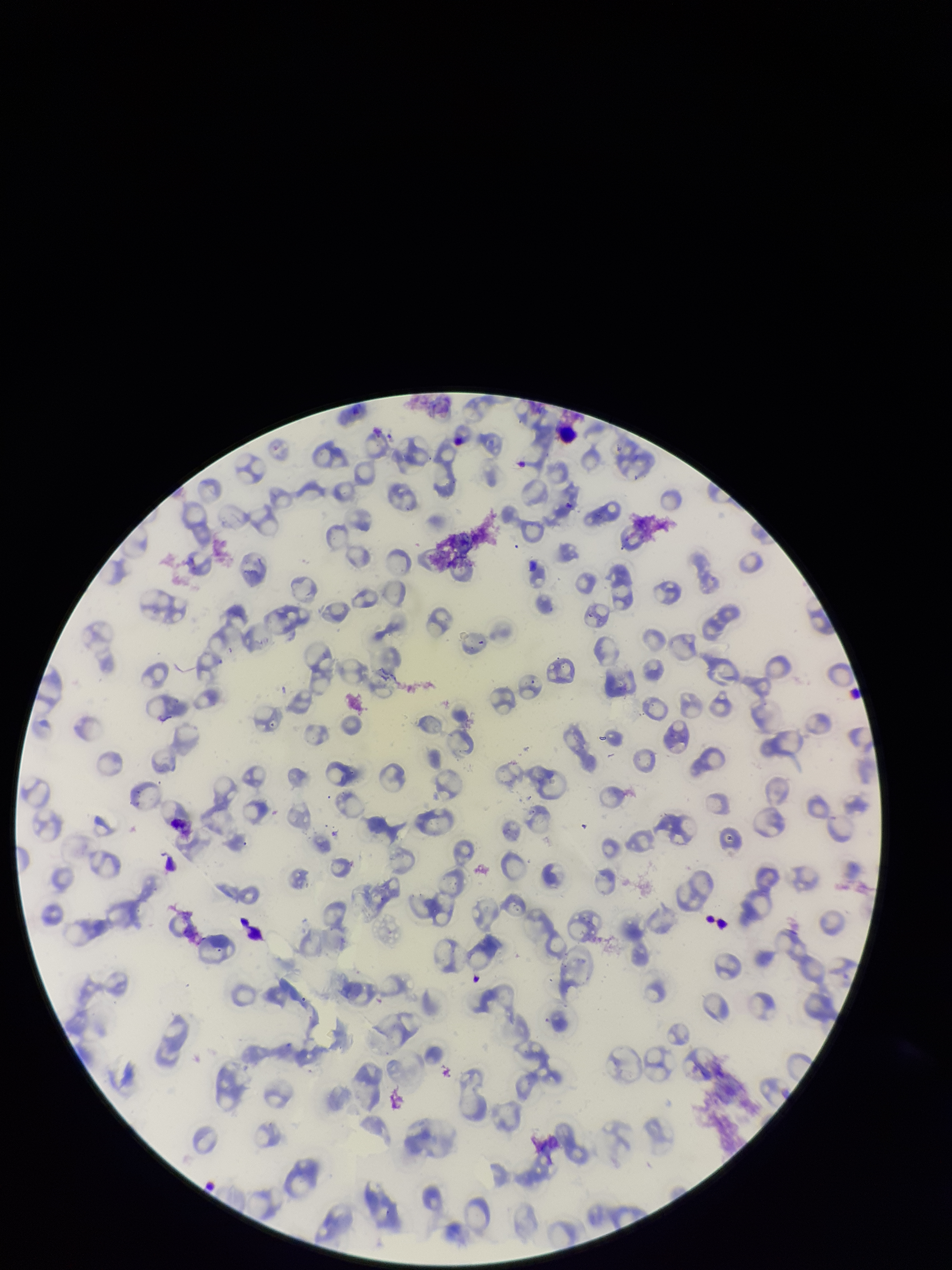 Stained with Giemsa. Image is 952×1270 pixels. Species reported for this patient: Plasmodium falciparum. Parasitized red blood cell count: 0. Preparation: thin blood smear. Red blood cell count: 101. Parasitized red blood cells: none detected. Single field of view. Smartphone photograph taken through the eyepiece of a microscope. Patient malaria status: infected.